Classify this cell by malaria status.
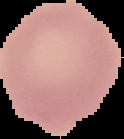
It is uninfected.

From a thin blood smear. Image is 124×139 pixels. Segmented cell region on a black background.